Locate every Plasmodium vivax-infected red blood cell.
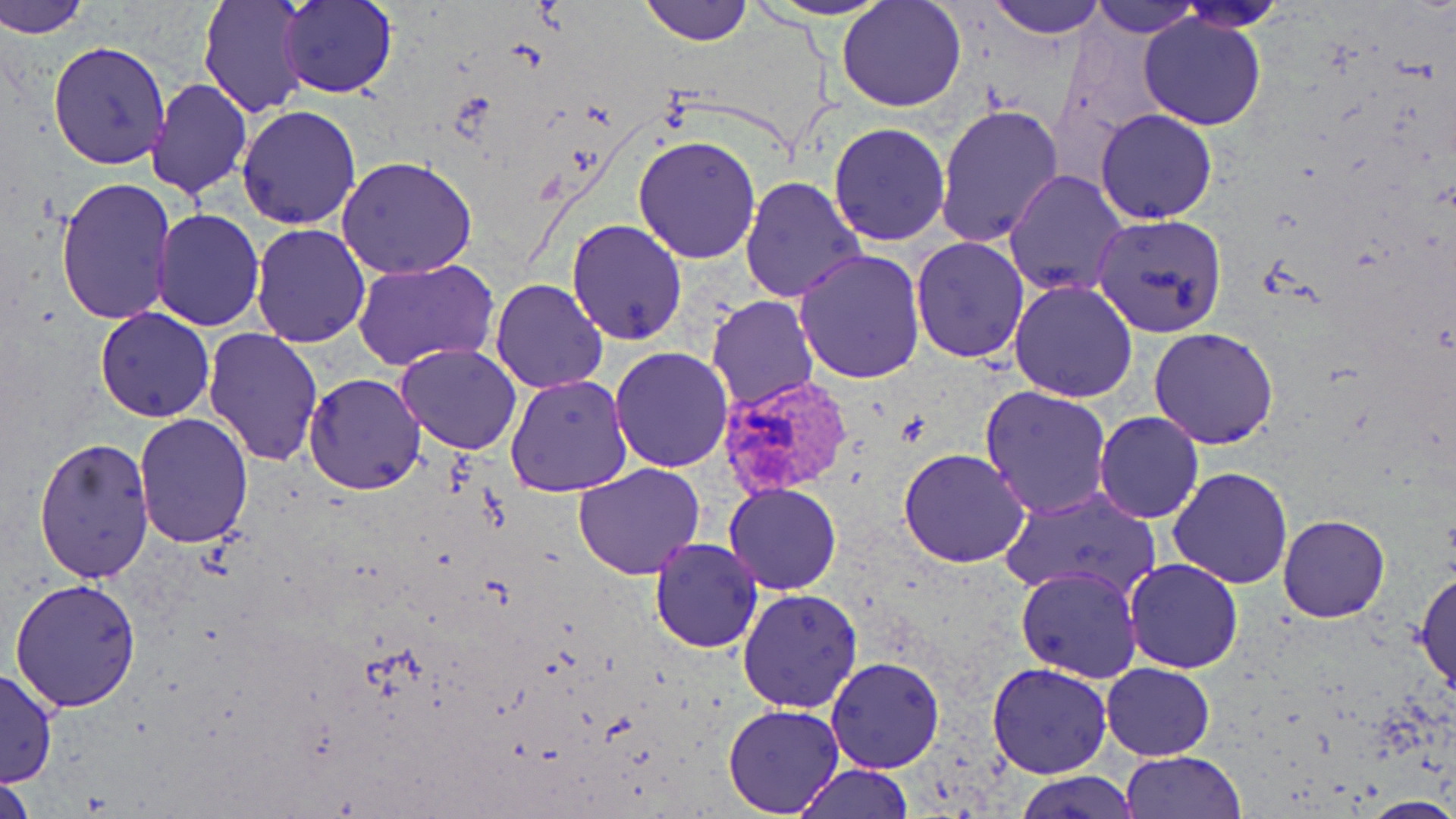
Approximate bounding boxes as (x1, y1, x2, y2) in pixels.
Plasmodium vivax-infected red blood cells: (718, 372, 854, 499).

Uninfected red blood cell locations: (1, 0, 92, 38), (198, 0, 310, 120), (279, 0, 398, 99), (640, 0, 751, 46), (761, 0, 895, 20), (836, 0, 968, 111), (989, 0, 1105, 38), (1090, 0, 1199, 38), (1177, 2, 1289, 32), (1138, 11, 1267, 131), (47, 40, 172, 171), (145, 78, 253, 200), (934, 101, 1064, 248), (235, 103, 362, 230), (1096, 108, 1219, 225), (829, 122, 949, 246), (633, 134, 764, 264), (337, 157, 478, 279), (1003, 169, 1129, 298), (740, 175, 866, 304), (54, 178, 179, 325), (153, 209, 265, 331), (1091, 213, 1228, 338), (567, 219, 687, 343), (250, 223, 373, 349), (911, 236, 1029, 364), (794, 248, 926, 384), (352, 259, 498, 370), (491, 277, 609, 394), (1008, 279, 1140, 403), (707, 295, 820, 411), (94, 307, 215, 422), (1150, 326, 1279, 448), (202, 329, 325, 466), (396, 344, 524, 455), (609, 347, 733, 471), (304, 372, 425, 495), (505, 373, 633, 497), (979, 386, 1112, 518), (132, 411, 254, 548), (1094, 412, 1204, 524), (35, 436, 156, 585), (900, 448, 1030, 568), (574, 463, 705, 580), (1167, 467, 1295, 587), (725, 483, 842, 596), (1002, 486, 1161, 602), (1277, 514, 1391, 622), (648, 537, 764, 654), (1124, 558, 1244, 674), (1016, 565, 1142, 683), (1414, 568, 1456, 695), (10, 578, 141, 711), (737, 588, 864, 714), (826, 655, 944, 773), (1101, 662, 1215, 760), (986, 663, 1113, 779), (0, 666, 57, 789), (723, 704, 846, 817), (1121, 751, 1245, 818), (793, 764, 913, 819), (0, 769, 36, 819), (1018, 771, 1137, 818), (1364, 796, 1456, 817). Slide-level diagnosis: Plasmodium vivax. One field of a larger specimen. Image is 1456×819 pixels. May-Grünwald-Giemsa-stained preparation. Thin blood smear. Optical microscopy. 1000x magnification.